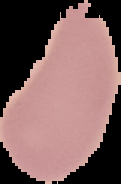

Image is 121×184 pixels. Segmented cell region on a black background. Result: no Plasmodium parasites detected. From a thin blood smear.